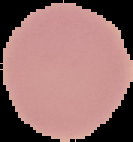

image_type: cell region segmented out of the field of view; surrounding area masked to black
result: negative for malaria parasites
preparation: thin blood smear
image_size: 133×142 pixels